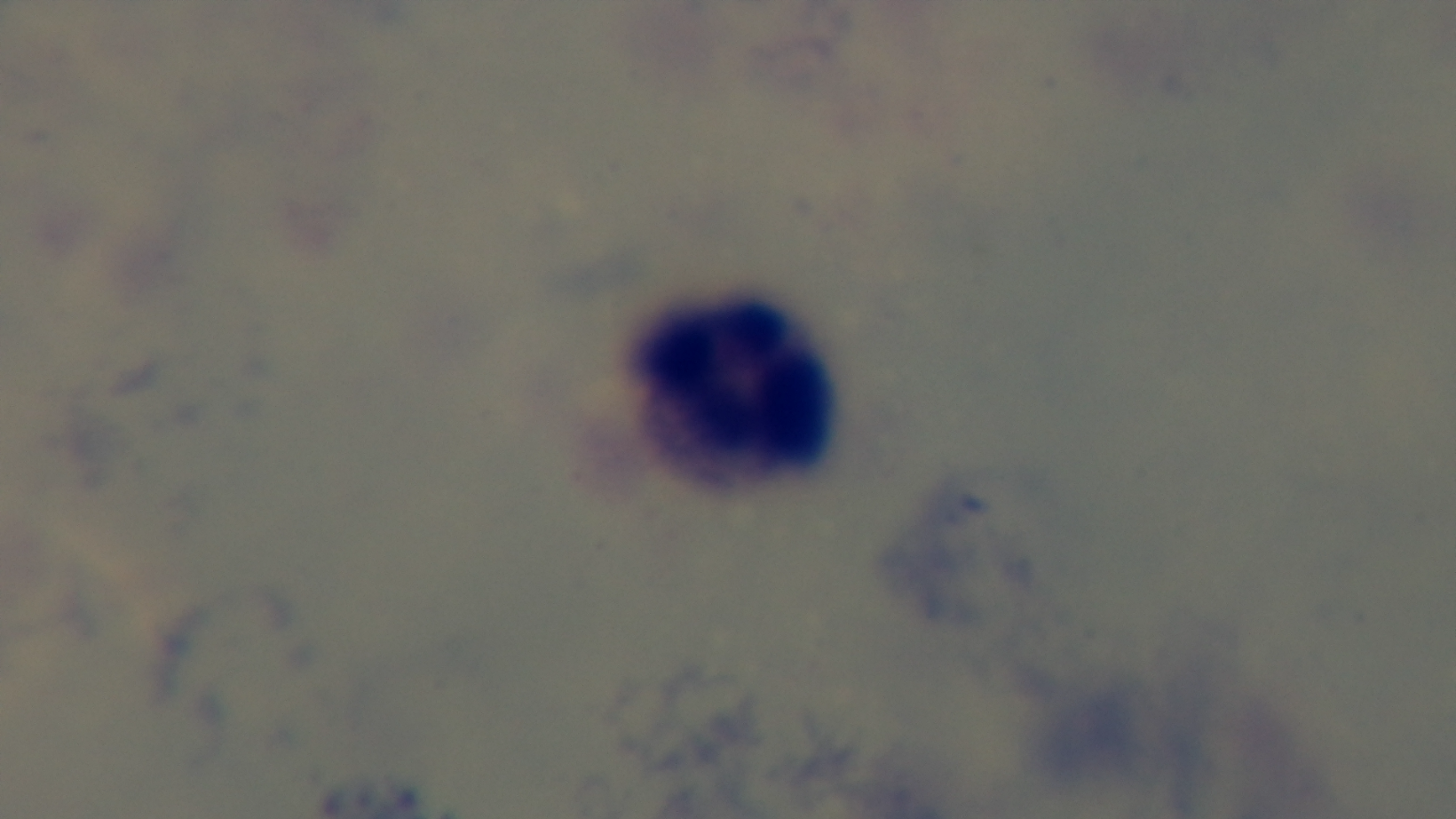
Preparation: thick smear. Malaria status: negative. Captured with a mounted 4K digital camera. Giemsa-stained. Oil-immersion objective, 100x. Light microscopy. Single field of view.